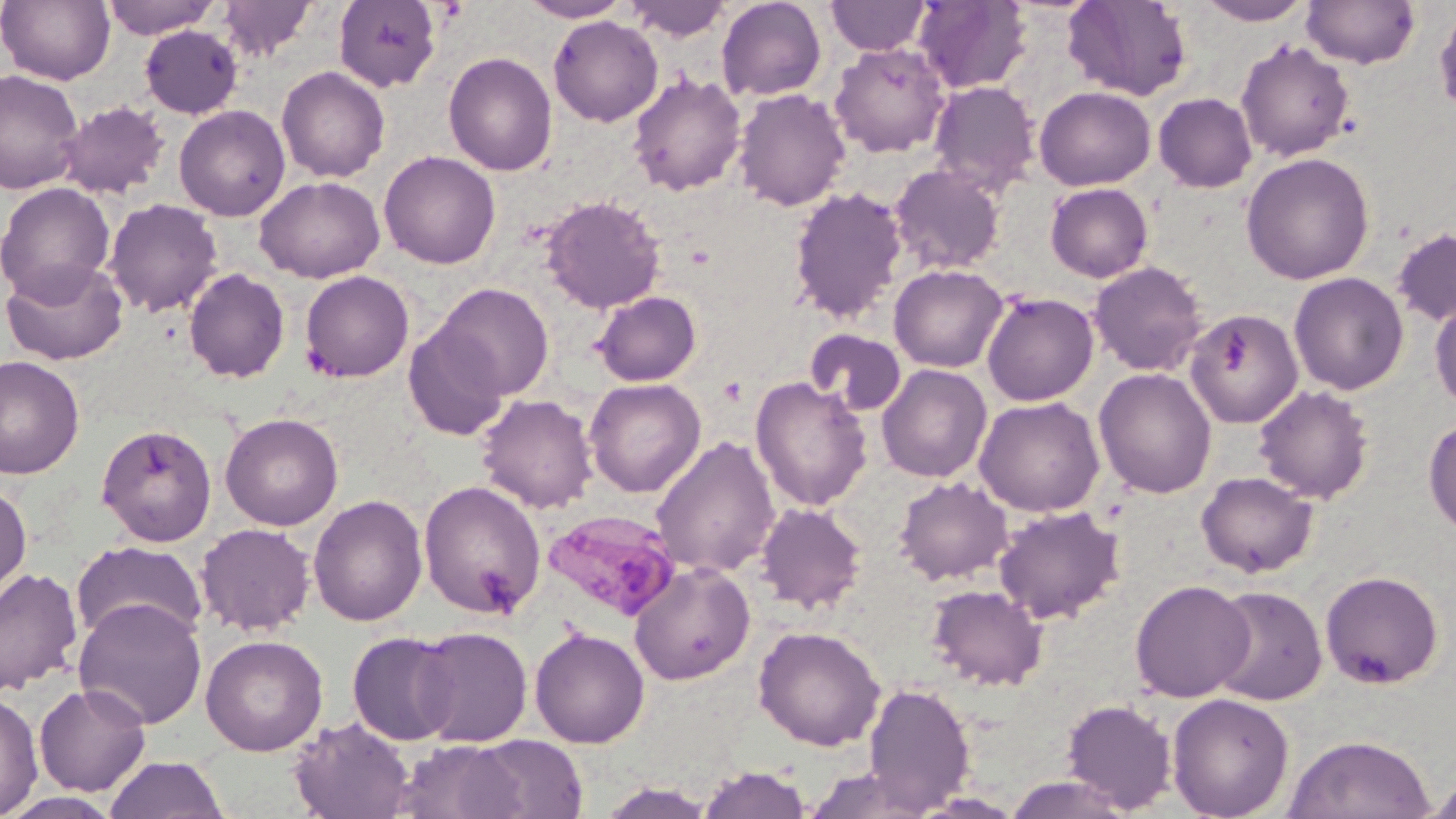
Summary:
  - Coordinate format: approximate bounding boxes as (x1, y1, x2, y2) in pixels
  - Plasmodium malariae-infected red blood cell locations: (541, 508, 680, 622)
  - Uninfected red blood cell locations: (0, 0, 115, 85), (101, 0, 220, 39), (217, 0, 317, 61), (333, 0, 442, 92), (518, 0, 634, 22), (625, 0, 730, 42), (716, 0, 827, 102), (1062, 0, 1192, 101), (1196, 0, 1314, 25), (1301, 0, 1420, 69), (826, 1, 932, 56), (913, 1, 1033, 93), (1433, 5, 1456, 119), (548, 16, 663, 127), (139, 24, 244, 120), (1236, 40, 1355, 162), (830, 42, 950, 157), (443, 51, 558, 176), (276, 66, 390, 183), (0, 69, 84, 195), (627, 72, 747, 197), (928, 80, 1041, 195), (1034, 86, 1156, 191), (733, 88, 851, 211), (1153, 92, 1257, 192), (58, 100, 170, 199), (174, 104, 291, 221), (379, 150, 501, 269), (1240, 152, 1375, 285), (889, 164, 1006, 275), (254, 175, 385, 282), (0, 182, 116, 305), (1045, 182, 1153, 283), (788, 187, 908, 324), (540, 194, 666, 314), (103, 198, 223, 318), (1391, 228, 1456, 327), (2, 258, 128, 365), (1089, 261, 1207, 377), (889, 264, 1009, 373), (184, 268, 290, 383), (299, 270, 414, 382), (1289, 272, 1409, 395), (434, 283, 554, 400), (592, 291, 702, 386), (981, 291, 1099, 406), (1429, 297, 1456, 413), (1186, 310, 1303, 429), (404, 323, 510, 441), (805, 329, 906, 417), (0, 355, 85, 479), (876, 364, 992, 483), (1094, 367, 1217, 499), (750, 376, 872, 512), (583, 378, 705, 498), (1254, 384, 1374, 504), (476, 393, 599, 514), (974, 396, 1104, 517), (219, 412, 343, 531), (1423, 416, 1456, 537), (95, 423, 218, 547), (650, 436, 780, 579), (1196, 471, 1318, 578), (894, 476, 1013, 585), (418, 480, 546, 619), (0, 481, 32, 602), (308, 494, 428, 626), (755, 501, 867, 614), (993, 506, 1125, 624), (195, 523, 316, 636), (71, 540, 207, 647), (628, 561, 755, 685), (0, 567, 83, 697), (1320, 570, 1444, 689), (1130, 579, 1255, 702), (927, 584, 1049, 691), (1209, 586, 1327, 705), (73, 597, 208, 730), (752, 625, 886, 751), (411, 626, 532, 747), (529, 626, 650, 748), (346, 631, 460, 746), (200, 634, 328, 756), (34, 682, 152, 796), (862, 682, 975, 813), (0, 690, 43, 819), (1166, 692, 1294, 819), (1061, 699, 1178, 813), (289, 716, 417, 819), (1283, 733, 1436, 819), (466, 736, 590, 817), (393, 739, 530, 819), (104, 754, 230, 819), (697, 764, 812, 818), (800, 768, 939, 819), (1421, 771, 1456, 817), (1001, 775, 1138, 818), (3, 791, 122, 818)
  - Slide-level diagnosis: Plasmodium malariae
  - Stain: May-Grünwald-Giemsa
  - Magnification: 1000x
  - Field of view: single
  - Modality: light microscopy
  - Preparation: thin blood film
  - Image size: 1456×819 pixels